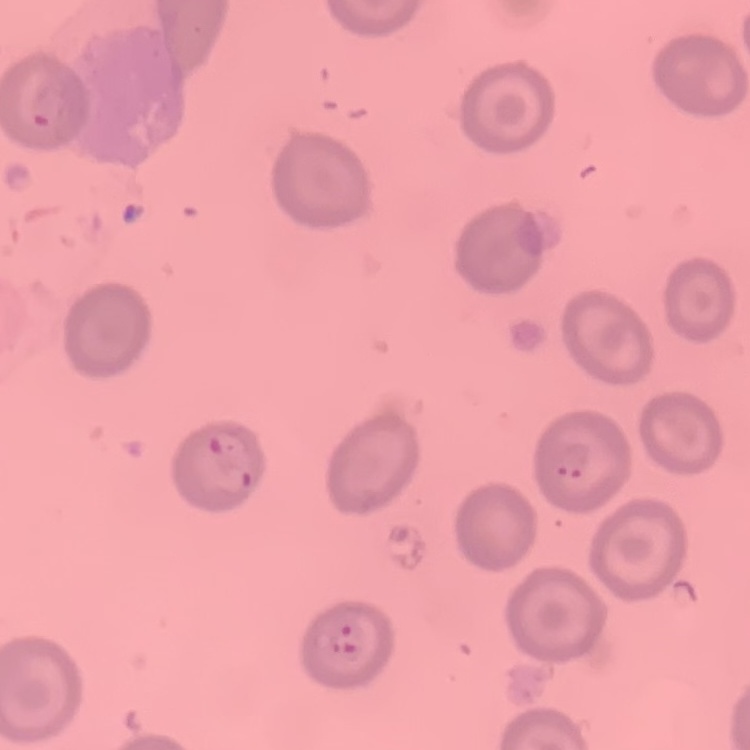
Summary:
  - Erythrocyte morphology: no rouleaux formation
  - Stain: Field's or Giemsa
  - Image type: square crop of a larger photomicrograph
  - Preparation: thin blood smear